Give the extent of all Plasmodium falciparum-infected red blood cells.
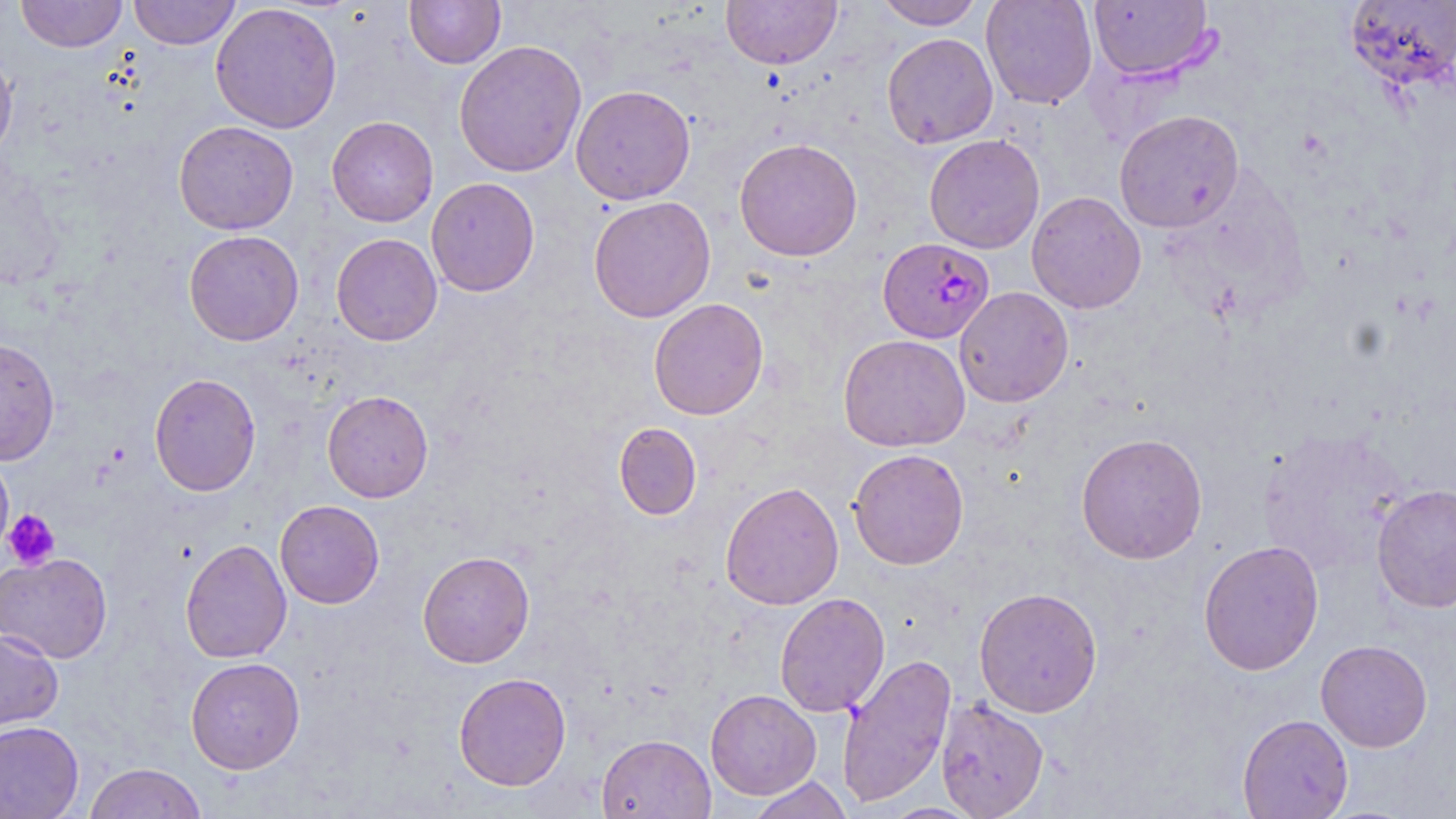
Approximate bounding boxes as (x1,y1)-(x2,y2) corner pairs in pixels.
Plasmodium falciparum-infected red blood cells: (878,237)-(995,343).

Platelet locations: (3,509)-(61,570). Uninfected red blood cell locations: (15,0)-(127,52), (128,0)-(242,49), (405,0)-(505,68), (720,0)-(842,70), (873,0)-(985,29), (981,0)-(1098,109), (1088,1)-(1216,82), (1344,1)-(1456,91), (210,2)-(342,134), (881,32)-(998,149), (453,40)-(587,177), (0,48)-(18,163), (571,84)-(696,205), (1114,109)-(1244,233), (327,115)-(439,227), (174,120)-(298,235), (924,134)-(1045,254), (734,138)-(863,261), (426,177)-(540,297), (1027,191)-(1146,313), (588,195)-(716,323), (184,229)-(304,346), (331,232)-(442,346), (954,286)-(1074,407), (648,297)-(769,420), (838,334)-(971,452), (0,338)-(60,465), (149,372)-(261,497), (322,390)-(433,503), (613,422)-(702,520), (1257,427)-(1410,577), (1076,432)-(1208,564), (848,448)-(969,569), (0,449)-(14,562), (720,481)-(844,610), (1371,483)-(1456,614), (275,500)-(385,608), (179,539)-(292,663), (1198,539)-(1324,676), (417,550)-(535,668), (0,552)-(112,663), (973,587)-(1103,717), (774,593)-(890,717), (0,628)-(64,735), (1315,639)-(1433,752), (837,653)-(956,808), (185,657)-(305,774), (453,672)-(572,791), (705,689)-(821,799), (936,698)-(1049,818), (1237,714)-(1354,819), (0,720)-(84,819), (597,733)-(716,819), (83,763)-(208,818), (746,776)-(854,818), (880,802)-(985,818). Slide-level diagnosis: Plasmodium falciparum. Image is 1456×819 pixels. Optical microscopy. May-Grünwald-Giemsa-stained preparation. One field of a larger specimen. 1000x magnification. Thin blood film.